Locate every Plasmodium parasite and every leukocyte.
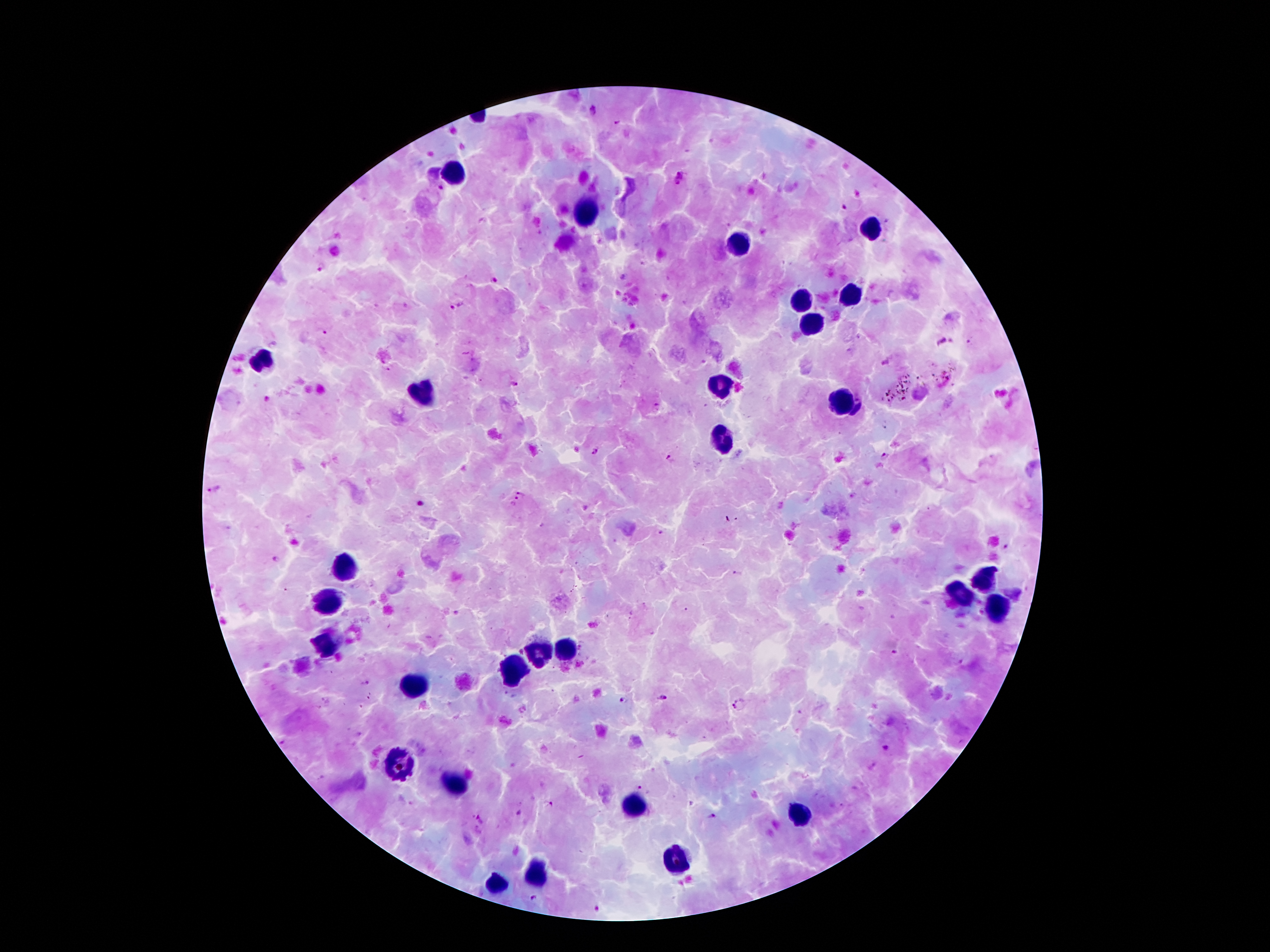

Approximate centers as {x, y} in pixels.
Plasmodium parasites: {593, 109}, {679, 178}, {442, 187}, {842, 207}, {321, 266}, {623, 275}, {494, 279}, {457, 305}, {323, 331}, {941, 341}, {390, 367}, {514, 384}, {658, 407}, {596, 450}, {884, 456}, {671, 460}, {214, 489}, {522, 494}, {514, 501}, {659, 532}, {1006, 547}, {276, 560}, {738, 575}, {892, 651}, {364, 683}, {664, 698}, {623, 699}, {738, 704}, {884, 748}, {641, 786}, {550, 803}, {518, 813}, {713, 816}, {480, 822}, {534, 897}, {598, 907}.
Leukocytes: {455, 173}, {582, 214}, {870, 227}, {738, 245}, {853, 294}, {800, 304}, {812, 325}, {260, 361}, {721, 386}, {425, 390}, {841, 400}, {725, 441}, {347, 566}, {985, 580}, {960, 592}, {332, 601}, {996, 609}, {327, 643}, {564, 652}, {538, 654}, {512, 668}, {411, 688}, {399, 760}, {449, 777}, {632, 807}, {802, 817}, {678, 860}, {536, 872}, {497, 884}.

Summary:
  - Stain: Giemsa
  - Preparation: thick peripheral-blood smear
  - Magnification: 100x
  - Field of view: one from this slide
  - Capture: smartphone through the microscope eyepiece
  - Image size: 1270×952 pixels
  - Patient malaria status: positive for Plasmodium falciparum